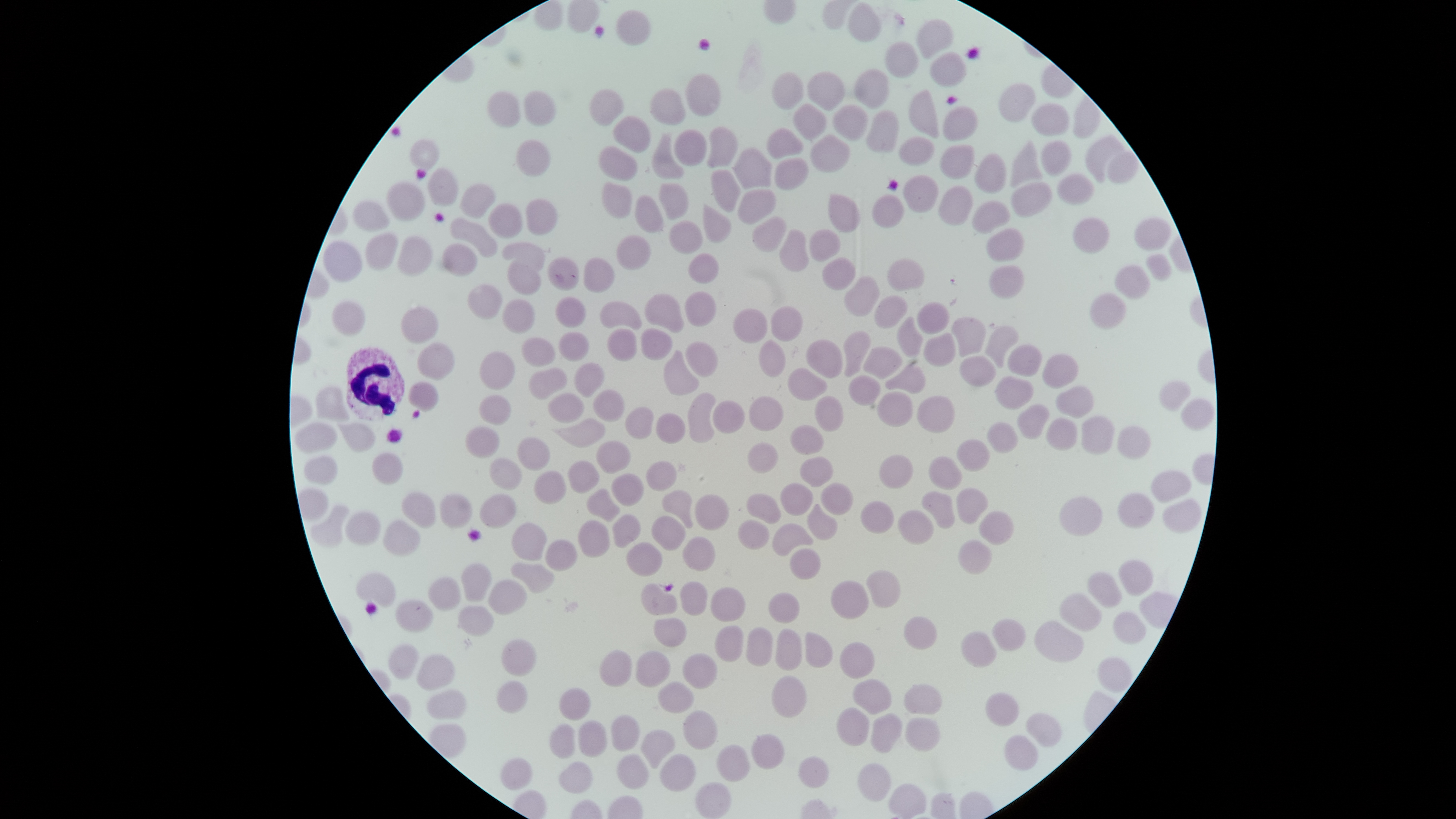

{
  "visible_region": "circular",
  "presence": "no malaria parasites identified",
  "image_size": "1456×819 pixels",
  "field_of_view": "single",
  "capture": "smartphone photograph through the microscope eyepiece",
  "uninfected_red_blood_cells": "approximate bounding boxes as (left, top, right, bottom) in pixels: (847, 2, 881, 42), (615, 9, 652, 46), (916, 18, 954, 59), (884, 41, 920, 78), (929, 52, 967, 87), (854, 68, 890, 109), (806, 71, 845, 110), (771, 72, 803, 110), (685, 73, 721, 117), (999, 82, 1036, 122), (589, 88, 624, 126), (648, 88, 686, 126), (908, 89, 939, 138), (524, 90, 556, 127), (487, 91, 520, 128), (1031, 102, 1070, 136), (793, 104, 826, 140), (833, 104, 868, 141), (942, 106, 978, 141), (866, 110, 900, 153), (613, 116, 650, 153), (707, 126, 738, 168), (766, 127, 803, 159), (673, 128, 707, 166), (651, 134, 684, 179), (1086, 134, 1124, 182), (810, 135, 850, 172), (899, 136, 934, 166), (410, 138, 440, 169), (515, 139, 551, 177), (1010, 140, 1043, 188), (1041, 140, 1072, 176), (940, 144, 975, 180), (598, 146, 638, 181), (734, 147, 771, 189), (1107, 150, 1139, 184), (974, 152, 1007, 194), (774, 157, 808, 191), (427, 167, 459, 207), (710, 169, 741, 213), (1056, 173, 1095, 206), (902, 175, 939, 213), (385, 180, 425, 222), (1011, 181, 1052, 217), (459, 182, 496, 219), (601, 182, 632, 218), (659, 182, 689, 220), (938, 185, 973, 226), (737, 188, 776, 224), (827, 193, 861, 233), (635, 194, 663, 234), (872, 194, 905, 228), (525, 198, 558, 236), (972, 200, 1010, 234), (352, 201, 391, 232), (488, 203, 523, 239), (703, 204, 731, 243), (751, 215, 786, 252), (1134, 217, 1171, 252), (449, 218, 498, 258), (1073, 218, 1109, 254), (669, 220, 703, 254), (809, 228, 841, 262), (986, 228, 1025, 262), (779, 229, 809, 272), (365, 233, 398, 271), (397, 235, 434, 276), (616, 235, 652, 270), (323, 240, 363, 282), (502, 241, 546, 270), (442, 243, 477, 277), (688, 252, 719, 284), (1145, 254, 1172, 281), (547, 257, 579, 291), (583, 257, 615, 293), (822, 257, 856, 290), (887, 258, 924, 291), (507, 259, 541, 295), (988, 264, 1025, 299), (1115, 265, 1150, 300), (844, 276, 880, 317), (466, 283, 503, 320), (685, 291, 716, 327), (644, 293, 685, 333), (1089, 293, 1126, 330), (874, 295, 908, 329), (555, 297, 586, 328), (501, 299, 535, 333), (332, 300, 366, 336), (599, 301, 643, 330), (917, 301, 950, 335), (770, 306, 803, 342), (401, 307, 439, 344), (732, 308, 767, 344), (896, 316, 924, 358), (952, 316, 986, 357), (985, 325, 1019, 368), (607, 327, 637, 362), (640, 328, 673, 361), (843, 331, 871, 378), (558, 332, 589, 362), (923, 332, 956, 367), (521, 337, 555, 367), (758, 339, 786, 378), (805, 339, 843, 379), (685, 341, 718, 377), (417, 342, 455, 381), (1007, 344, 1043, 378), (863, 346, 902, 379), (663, 349, 699, 396), (479, 351, 515, 391), (1042, 354, 1079, 389), (959, 356, 996, 387), (573, 362, 604, 398), (885, 364, 926, 394), (787, 367, 828, 401), (529, 368, 567, 400), (848, 375, 881, 406), (995, 376, 1035, 410), (408, 381, 439, 413), (1158, 381, 1190, 412), (1055, 385, 1094, 419), (315, 386, 350, 421), (592, 389, 624, 422), (877, 391, 914, 427), (687, 392, 716, 443), (548, 393, 584, 424), (479, 395, 511, 425), (748, 395, 784, 431), (916, 395, 955, 434), (815, 396, 844, 432), (1180, 398, 1215, 430), (713, 400, 745, 434), (1017, 404, 1050, 439), (624, 406, 654, 439), (655, 412, 686, 445), (1081, 416, 1115, 456), (1046, 417, 1078, 451), (553, 418, 605, 449), (336, 421, 376, 452), (294, 422, 338, 454), (987, 422, 1018, 453), (465, 425, 500, 459), (789, 425, 824, 456), (1116, 425, 1151, 460), (517, 437, 551, 472), (956, 439, 990, 472), (595, 440, 631, 474), (747, 442, 778, 473), (372, 452, 403, 485), (879, 454, 914, 489), (304, 455, 338, 485), (799, 456, 834, 487), (928, 456, 963, 490), (489, 457, 523, 490), (567, 460, 600, 494), (645, 460, 677, 491), (533, 470, 567, 504), (1151, 471, 1191, 502), (611, 473, 644, 507), (821, 482, 854, 515), (779, 483, 813, 516), (956, 487, 989, 525), (587, 488, 621, 523), (662, 489, 694, 529), (922, 490, 955, 530), (401, 491, 436, 529), (1116, 492, 1154, 528), (439, 493, 473, 529), (479, 493, 517, 529), (746, 493, 781, 524), (695, 494, 729, 531), (1059, 496, 1103, 537), (1161, 498, 1202, 534), (860, 501, 894, 534), (807, 503, 838, 541), (310, 505, 349, 547), (897, 509, 934, 545), (979, 510, 1014, 546), (344, 511, 380, 545), (612, 513, 641, 548), (651, 515, 686, 551), (737, 518, 769, 550), (382, 519, 421, 556), (577, 520, 610, 559), (511, 522, 547, 562), (771, 522, 814, 556), (682, 536, 716, 572), (545, 539, 578, 572), (958, 539, 993, 576), (626, 542, 663, 577), (790, 548, 821, 580), (1117, 559, 1154, 596), (461, 562, 492, 602), (511, 562, 554, 594), (866, 569, 900, 608), (1086, 571, 1122, 608), (356, 573, 396, 608), (428, 576, 461, 611), (488, 579, 527, 616), (830, 580, 869, 620), (680, 581, 707, 616), (640, 583, 678, 616), (710, 586, 747, 622), (767, 592, 801, 623), (1058, 593, 1102, 631), (395, 600, 434, 633), (458, 605, 494, 637), (1112, 610, 1147, 645), (903, 616, 938, 649), (653, 617, 687, 647), (992, 618, 1026, 651), (1034, 620, 1084, 662), (714, 625, 743, 661), (746, 626, 773, 666), (775, 628, 802, 670), (804, 631, 833, 668), (961, 631, 997, 668), (501, 639, 536, 676), (838, 641, 875, 678), (388, 643, 419, 679), (599, 649, 632, 687), (635, 650, 672, 689), (682, 653, 718, 689), (416, 654, 456, 691), (771, 675, 807, 718), (852, 678, 892, 714), (497, 680, 528, 713), (658, 681, 694, 714), (903, 684, 944, 715), (558, 688, 591, 720), (427, 689, 466, 720), (985, 691, 1020, 726), (836, 707, 869, 746), (683, 710, 719, 750), (870, 712, 902, 753), (1025, 712, 1062, 747), (611, 715, 639, 752), (905, 716, 941, 752), (578, 719, 607, 757), (549, 723, 575, 759), (641, 730, 675, 769), (750, 733, 784, 770), (1003, 735, 1039, 770), (716, 743, 751, 782), (616, 753, 649, 789), (659, 753, 696, 792), (501, 756, 533, 790), (798, 756, 830, 789), (558, 761, 592, 794), (858, 762, 891, 801), (695, 782, 732, 818), (888, 783, 927, 818)",
  "preparation": "thin blood film",
  "white_blood_cells": "approximate bounding boxes as (left, top, right, bottom) in pixels: (346, 347, 406, 420)",
  "stain": "Giemsa"
}